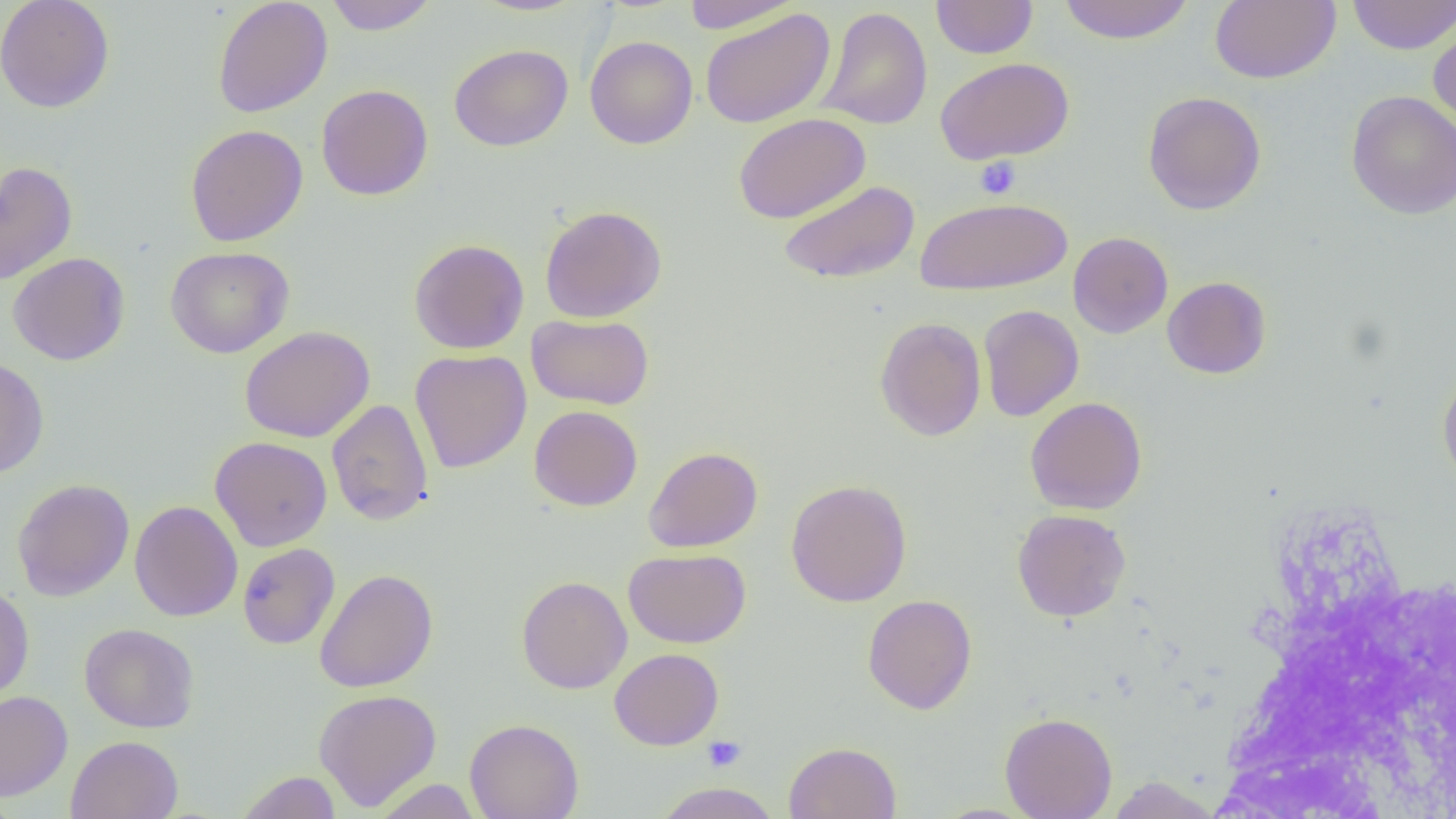 Approximate bounding boxes as (x1,y1)-(x2,y2) corner pairs in pixels. Platelet locations: (975,156)-(1021,199), (703,736)-(746,772). Uninfected red blood cell locations: (0,0)-(115,113), (212,0)-(332,117), (324,0)-(439,35), (471,0)-(588,16), (682,0)-(803,33), (931,0)-(1038,58), (1058,0)-(1196,44), (1210,0)-(1340,84), (1347,0)-(1456,55), (816,6)-(933,130), (700,8)-(836,128), (1427,18)-(1456,132), (585,36)-(698,149), (449,44)-(573,151), (935,57)-(1074,164), (316,84)-(433,200), (1345,89)-(1456,220), (1142,91)-(1266,215), (732,113)-(870,224), (185,124)-(308,246), (0,160)-(77,285), (779,180)-(920,285), (915,197)-(1072,295), (540,205)-(667,322), (1068,232)-(1173,338), (408,239)-(529,354), (165,246)-(295,358), (7,251)-(130,366), (1162,276)-(1271,379), (979,305)-(1084,422), (526,313)-(654,410), (874,317)-(987,441), (240,325)-(375,443), (410,349)-(532,473), (0,357)-(49,478), (1437,368)-(1456,493), (1025,396)-(1148,515), (326,399)-(434,526), (529,405)-(643,511), (210,436)-(332,551), (643,446)-(763,552), (12,478)-(134,601), (785,479)-(912,607), (130,500)-(243,622), (1012,509)-(1131,622), (238,543)-(340,649), (623,548)-(751,648), (314,568)-(438,692), (516,575)-(632,694), (0,583)-(34,703), (862,594)-(977,715), (79,623)-(200,733), (609,648)-(724,750), (313,689)-(442,812), (0,691)-(73,801), (1000,712)-(1117,818), (464,718)-(584,819), (66,735)-(183,819), (784,741)-(902,819), (235,771)-(343,818), (1104,776)-(1223,818), (372,779)-(482,819), (652,782)-(782,818), (928,804)-(1041,819). Slide-level diagnosis: no evidence of blood parasites. One field of a larger specimen. 1000x magnification. Image is 1456×819 pixels. Optical microscopy. Thin blood film.